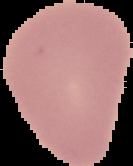

Summary:
  - Image size: 133×166 pixels
  - Preparation: thin blood film
  - Image type: segmented cell region on a black background
  - Malaria status: uninfected